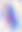

Summary:
  - Identification: Toxoplasma gondii
  - Modality: micrograph
  - Magnification: 400x